Classify this cell by malaria status.
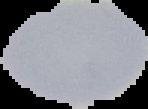
It is parasitized.

preparation = thin blood film
image type = segmented cell region on a black background
image size = 148×109 pixels